Outline each blood parasite and name the species.
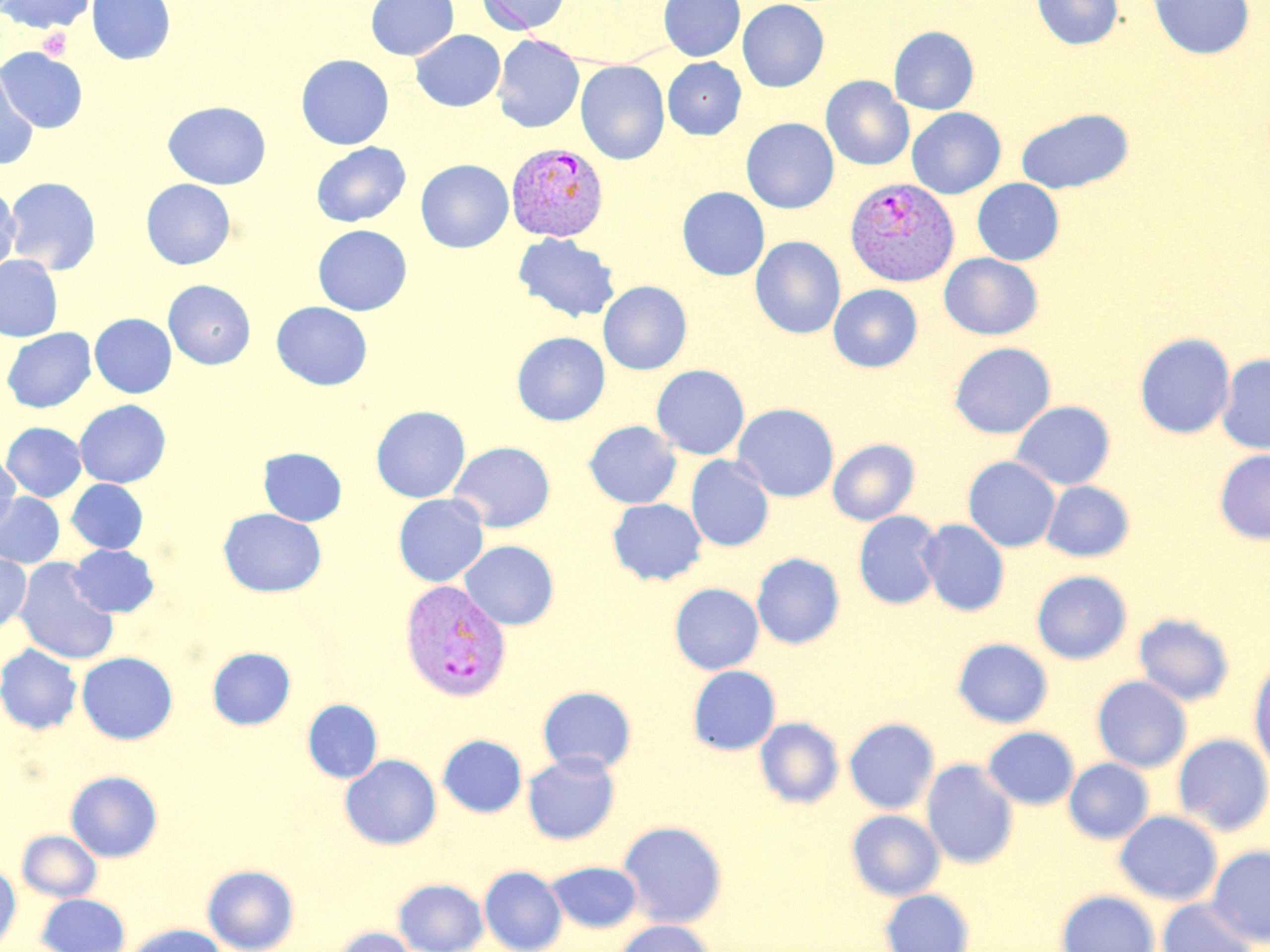

Approximate bounding boxes as (x1, y1, x2, y2) in pixels.
Plasmodium vivax-infected red blood cells: (506, 142, 609, 241), (845, 177, 958, 286), (399, 580, 511, 701).
No Plasmodium falciparum, Plasmodium ovale, Plasmodium malariae, Babesia divergens, or Trypanosoma brucei observed.

slide-level diagnosis = Plasmodium vivax
field of view = one of a larger specimen
image size = 1270×952 pixels
modality = optical microscopy
magnification = 1000x
preparation = thin blood film
uninfected red blood cell locations = approximate bounding boxes as (x1, y1, x2, y2) in pixels: (3, 0, 96, 34), (87, 0, 175, 65), (365, 0, 458, 60), (477, 0, 570, 35), (659, 0, 744, 61), (737, 0, 829, 92), (1032, 0, 1123, 50), (1148, 0, 1254, 59), (889, 26, 979, 115), (410, 30, 505, 112), (492, 35, 584, 133), (0, 47, 88, 133), (296, 54, 394, 149), (663, 57, 746, 139), (575, 60, 669, 165), (0, 65, 39, 171), (821, 76, 914, 170), (163, 101, 271, 190), (907, 108, 1006, 199), (1016, 108, 1133, 194), (741, 118, 839, 213), (311, 142, 411, 227), (416, 159, 513, 252), (4, 177, 102, 275), (972, 178, 1064, 265), (140, 179, 236, 270), (0, 185, 20, 277), (677, 187, 770, 281), (312, 224, 412, 315), (513, 233, 620, 323), (750, 236, 845, 339), (939, 253, 1042, 340), (0, 255, 63, 342), (163, 280, 256, 369), (598, 281, 692, 375), (828, 284, 922, 372), (272, 301, 372, 390), (90, 313, 176, 398), (1, 327, 96, 412), (512, 332, 610, 425), (1135, 332, 1235, 439), (949, 342, 1056, 438), (1217, 354, 1270, 454), (651, 364, 749, 459), (75, 399, 171, 488), (1011, 401, 1115, 490), (732, 403, 839, 502), (371, 405, 470, 502), (584, 420, 681, 509), (2, 422, 87, 501), (828, 438, 919, 525), (448, 441, 555, 532), (259, 448, 347, 526), (1215, 450, 1270, 544), (0, 455, 20, 534), (685, 455, 774, 552), (963, 456, 1060, 552), (67, 479, 147, 553), (1042, 481, 1135, 562), (0, 492, 64, 568), (393, 494, 488, 587), (607, 498, 707, 585), (218, 508, 326, 597), (853, 510, 944, 610), (918, 519, 1009, 616), (459, 540, 559, 630), (69, 544, 159, 617), (0, 553, 31, 634), (751, 553, 845, 649), (14, 558, 119, 665), (1032, 570, 1132, 664), (670, 583, 764, 674), (1134, 613, 1235, 706), (952, 638, 1053, 727), (0, 643, 83, 735), (207, 647, 295, 729), (77, 652, 177, 744), (1248, 658, 1270, 777), (687, 665, 781, 755), (1091, 676, 1192, 772), (537, 686, 637, 775), (302, 699, 382, 783), (754, 717, 844, 808), (843, 717, 940, 814), (982, 727, 1079, 810), (437, 734, 526, 817), (1172, 734, 1270, 835), (523, 752, 620, 844), (340, 754, 441, 849), (1063, 758, 1154, 844), (921, 759, 1018, 868), (66, 770, 162, 862), (846, 809, 945, 900), (1114, 810, 1222, 906), (617, 820, 728, 928), (17, 830, 102, 902), (1207, 845, 1270, 946), (545, 860, 642, 933), (0, 864, 21, 951), (202, 864, 299, 952), (479, 866, 566, 952), (393, 878, 488, 952), (880, 889, 975, 952), (1056, 890, 1160, 952), (36, 893, 130, 952), (1157, 899, 1258, 952), (612, 920, 716, 952), (124, 923, 228, 952), (329, 926, 420, 952)
stain = May-Grünwald-Giemsa
platelet locations = approximate bounding boxes as (x1, y1, x2, y2) in pixels: (38, 27, 73, 60)